Report the malaria status of this cell.
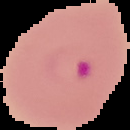

Parasitized.

Summary:
  - Image type: segmented cell region with the area outside set to black
  - Image size: 130×130 pixels
  - Preparation: thin blood smear